Assess this cell for malaria.
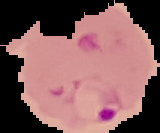

It is parasitized.

image_size: 160×133 pixels
image_type: cell region segmented out of the field of view; surrounding area masked to black
preparation: thin blood smear